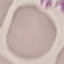

malaria status = uninfected
image type = automatically extracted cell patch, resized to 64 × 64 pixels
preparation = thin blood smear
capture = smartphone through the microscope eyepiece
stain = Giemsa